Identify the preparation type.
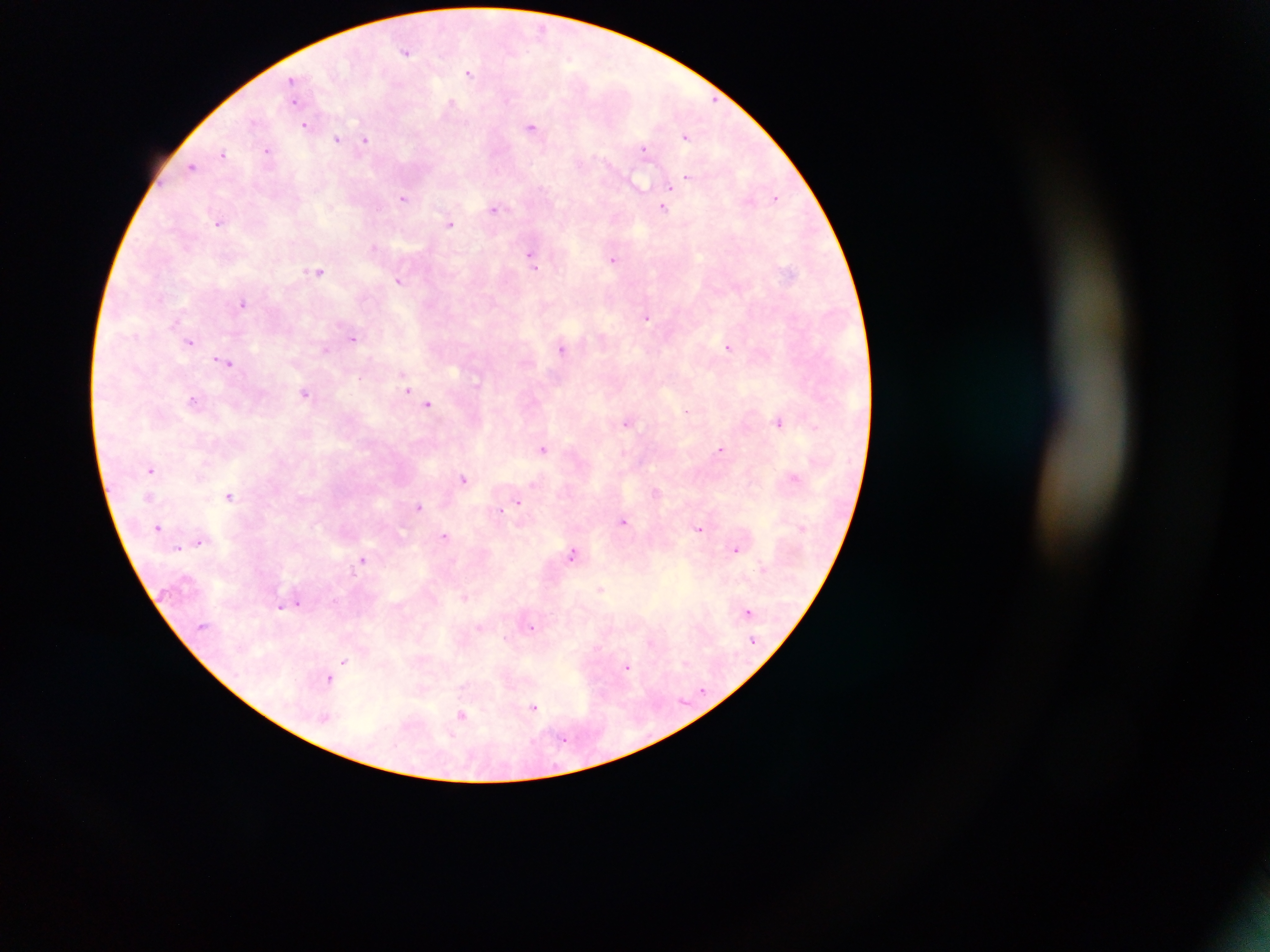
Thick blood film.

Approximate centers as x y in pixels. Malaria parasite locations: 541 30; 406 51; 570 59; 468 72; 292 79; 294 100; 508 100; 450 104; 254 122; 304 125; 531 127; 685 137; 337 139; 365 141; 643 148; 268 150; 223 153; 191 167; 687 178; 639 183; 671 187; 776 197; 404 198; 664 208; 494 209; 219 222; 450 224; 374 246; 531 254; 613 259; 533 266; 319 272; 399 281; 160 299; 243 303; 647 318; 353 338; 189 342; 728 347; 562 348; 326 349; 226 363; 360 378; 405 381; 407 390; 305 393; 192 400; 428 404; 686 411; 626 422; 779 422; 816 427; 543 448; 720 450; 151 469; 463 478; 793 478; 532 485; 656 492; 229 495; 148 496; 518 502; 419 506; 500 511; 623 521; 158 527; 700 528; 444 535; 198 541; 178 548; 736 549; 573 554; 363 559; 762 566; 601 589; 465 597; 298 603; 280 607; 747 611; 531 627; 505 637; 650 642; 345 661; 686 662; 627 668; 329 679; 534 707; 461 716; 325 719; 564 739. Mobile-phone photograph taken through the microscope. Single field of view. Sample from Ghana. Image is 1270×952 pixels.